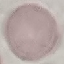
result = no malaria parasites detected
stain = Giemsa
preparation = thin blood smear
capture = smartphone camera at the microscope eyepiece
image type = cell patch, automatically extracted from a larger field of view and resized to 64 × 64 pixels